Point out each leukocyte.
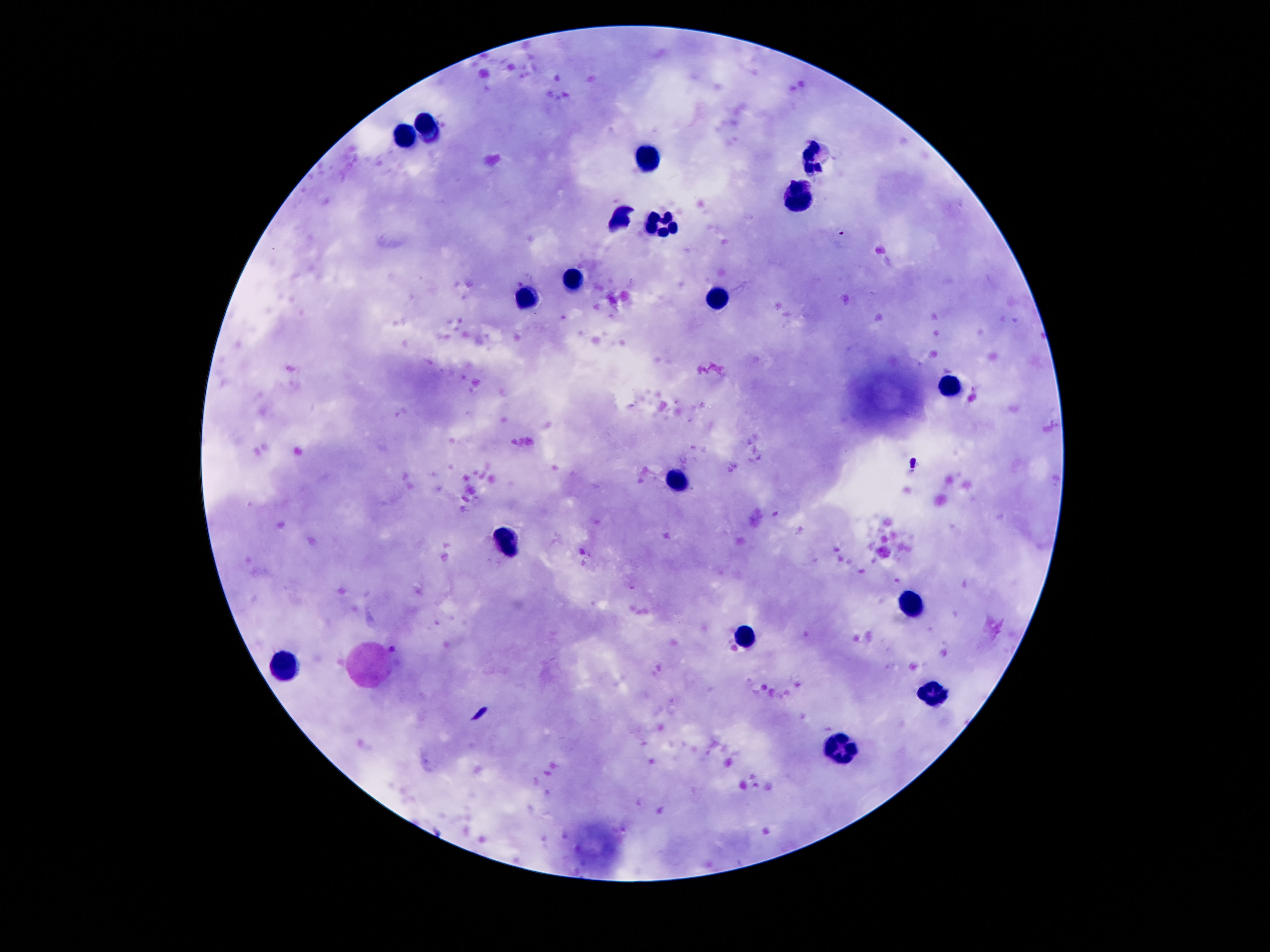

Approximate centers as [x, y] in pixels.
Leukocytes: [427, 123], [405, 136], [819, 156], [646, 159], [797, 194], [618, 216], [659, 227], [571, 283], [524, 298], [717, 300], [950, 385], [674, 481], [506, 543], [909, 601], [745, 636], [287, 662], [931, 693], [840, 748].

{
  "image_size": "1270×952 pixels",
  "capture": "smartphone camera through the microscope eyepiece",
  "patient_malaria_status": "uninfected",
  "magnification": "100x",
  "field_of_view": "one from this slide",
  "preparation": "thick blood smear",
  "stain": "Giemsa"
}